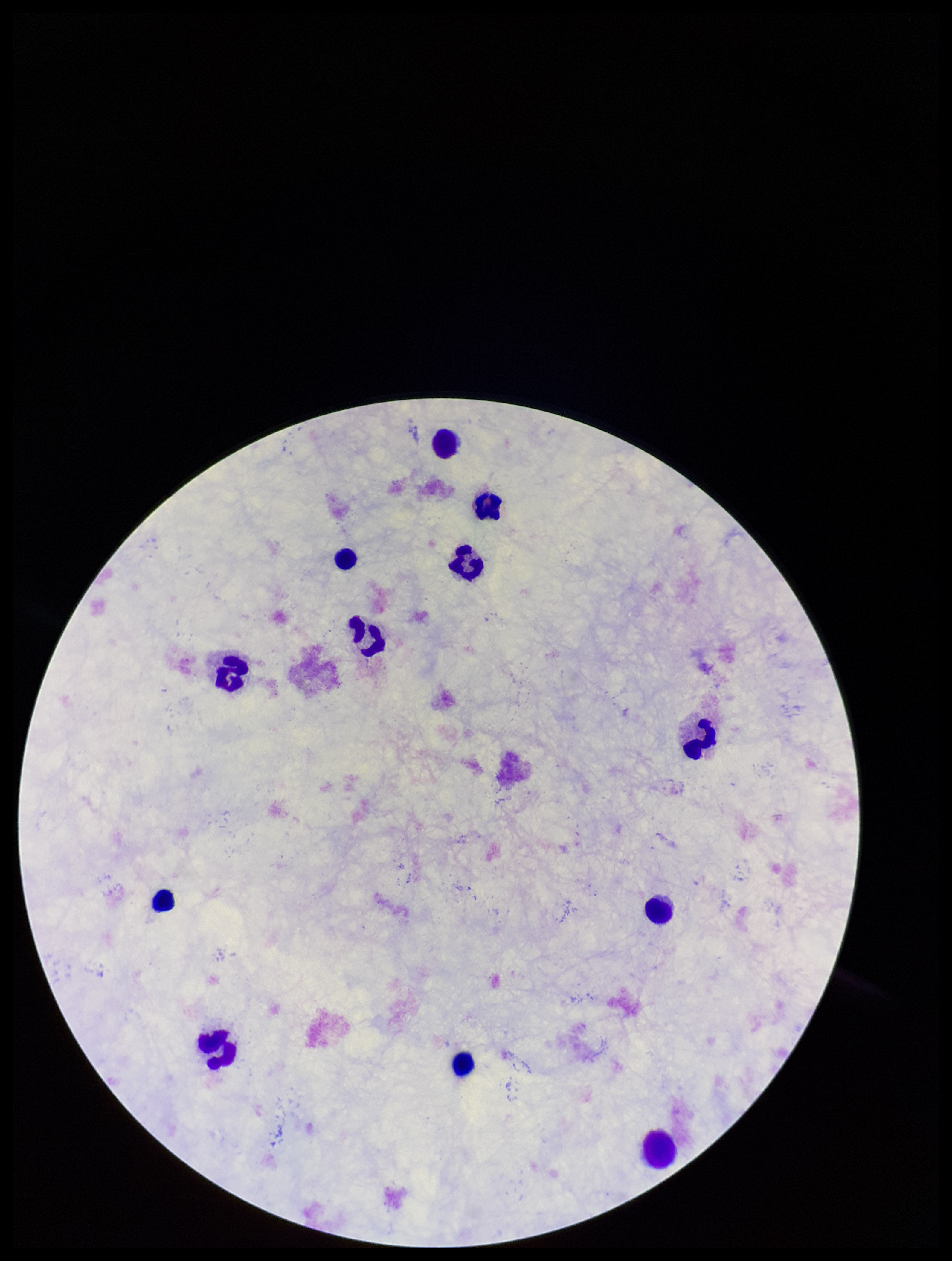

preparation = thick
stain = Giemsa
patient malaria status = negative
leukocyte count = 12
capture = smartphone photograph through the microscope eyepiece
image size = 952×1261 pixels
field of view = one from this slide
parasite count = 0
Plasmodium parasites = none detected